Locate and identify every blood parasite.
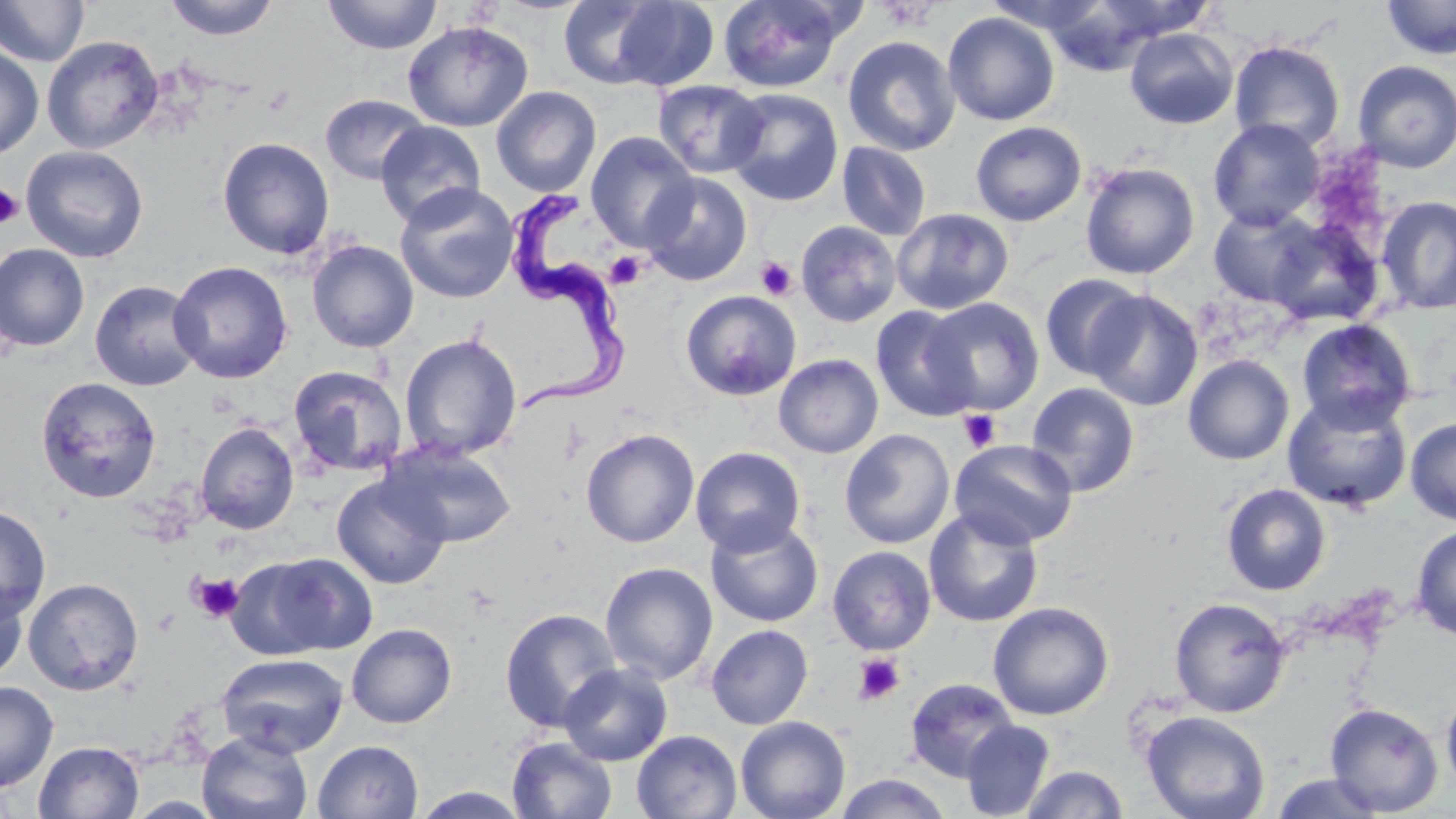
Approximate bounding boxes as [x1, y1, x2, y2] in pixels.
Trypanosoma brucei: [500, 191, 633, 418].
No Plasmodium falciparum, Plasmodium ovale, Plasmodium malariae, Plasmodium vivax, or Babesia divergens observed.

{
  "slide_level_diagnosis": "Trypanosoma brucei",
  "uninfected_red_blood_cell_locations": "approximate bounding boxes as [x1, y1, x2, y2] in pixels: [164, 0, 279, 41], [322, 0, 442, 55], [559, 0, 667, 88], [717, 0, 850, 93], [1034, 0, 1169, 76], [1076, 0, 1219, 44], [1381, 0, 1456, 60], [0, 1, 90, 67], [610, 1, 720, 90], [942, 12, 1060, 126], [403, 21, 533, 132], [1124, 27, 1238, 129], [42, 36, 163, 154], [842, 36, 961, 156], [1228, 39, 1346, 152], [0, 46, 43, 160], [1352, 60, 1456, 173], [652, 80, 768, 178], [491, 86, 602, 197], [723, 88, 844, 207], [320, 94, 430, 184], [1208, 118, 1324, 231], [376, 121, 487, 227], [970, 121, 1086, 226], [585, 132, 698, 251], [217, 137, 335, 260], [837, 141, 932, 241], [21, 145, 149, 263], [1079, 162, 1199, 279], [641, 172, 752, 286], [394, 182, 519, 305], [1376, 195, 1456, 315], [1208, 205, 1322, 307], [891, 208, 1014, 315], [1265, 219, 1384, 327], [796, 221, 902, 327], [306, 239, 419, 353], [0, 244, 90, 351], [168, 260, 293, 384], [1039, 275, 1147, 381], [89, 279, 203, 391], [680, 290, 802, 401], [1084, 290, 1203, 411], [920, 298, 1045, 415], [871, 305, 980, 422], [1296, 318, 1417, 433], [399, 333, 522, 462], [773, 354, 883, 458], [1183, 354, 1294, 465], [288, 364, 409, 477], [35, 376, 161, 503], [1026, 383, 1140, 497], [1282, 393, 1413, 513], [1405, 418, 1456, 525], [195, 421, 299, 534], [580, 429, 700, 548], [839, 429, 955, 548], [949, 439, 1078, 549], [380, 440, 517, 548], [690, 446, 806, 556], [331, 474, 450, 589], [1221, 483, 1331, 596], [0, 505, 51, 622], [924, 507, 1045, 628], [705, 517, 823, 628], [1410, 524, 1456, 640], [827, 545, 936, 655], [249, 552, 378, 656], [599, 561, 719, 685], [23, 577, 144, 695], [0, 582, 28, 683], [1169, 597, 1291, 718], [987, 601, 1115, 721], [499, 607, 621, 732], [346, 623, 457, 728], [706, 624, 813, 730], [216, 652, 349, 757], [558, 662, 673, 766], [905, 677, 1019, 782], [0, 681, 59, 792], [1441, 683, 1456, 798], [1324, 702, 1444, 816], [1142, 711, 1270, 819], [735, 716, 851, 819], [960, 720, 1057, 818], [197, 730, 313, 818], [631, 730, 742, 818], [507, 737, 618, 819], [312, 739, 423, 819], [34, 740, 144, 819], [1020, 765, 1130, 818], [1269, 772, 1388, 818], [833, 773, 954, 819], [409, 787, 533, 819]",
  "field_of_view": "one of a larger specimen",
  "stain": "May-Grünwald-Giemsa",
  "platelet_locations": "approximate bounding boxes as [x1, y1, x2, y2] in pixels: [881, 2, 940, 31], [0, 183, 24, 229], [606, 251, 647, 289], [755, 256, 798, 301], [959, 409, 1001, 452], [190, 571, 245, 623], [853, 653, 906, 705]",
  "modality": "light microscopy",
  "magnification": "1000x",
  "preparation": "thin blood smear",
  "image_size": "1456×819 pixels"
}